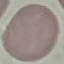
result: negative for malaria parasites
stain: Giemsa
capture: smartphone through the microscope eyepiece
preparation: thin blood film
image_type: cell patch, automatically extracted from a larger field of view and resized to 64 × 64 pixels